Name the cell type shown.
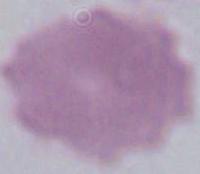

An erythrocyte.

{
  "modality": "photomicrograph",
  "magnification": "1000x"
}